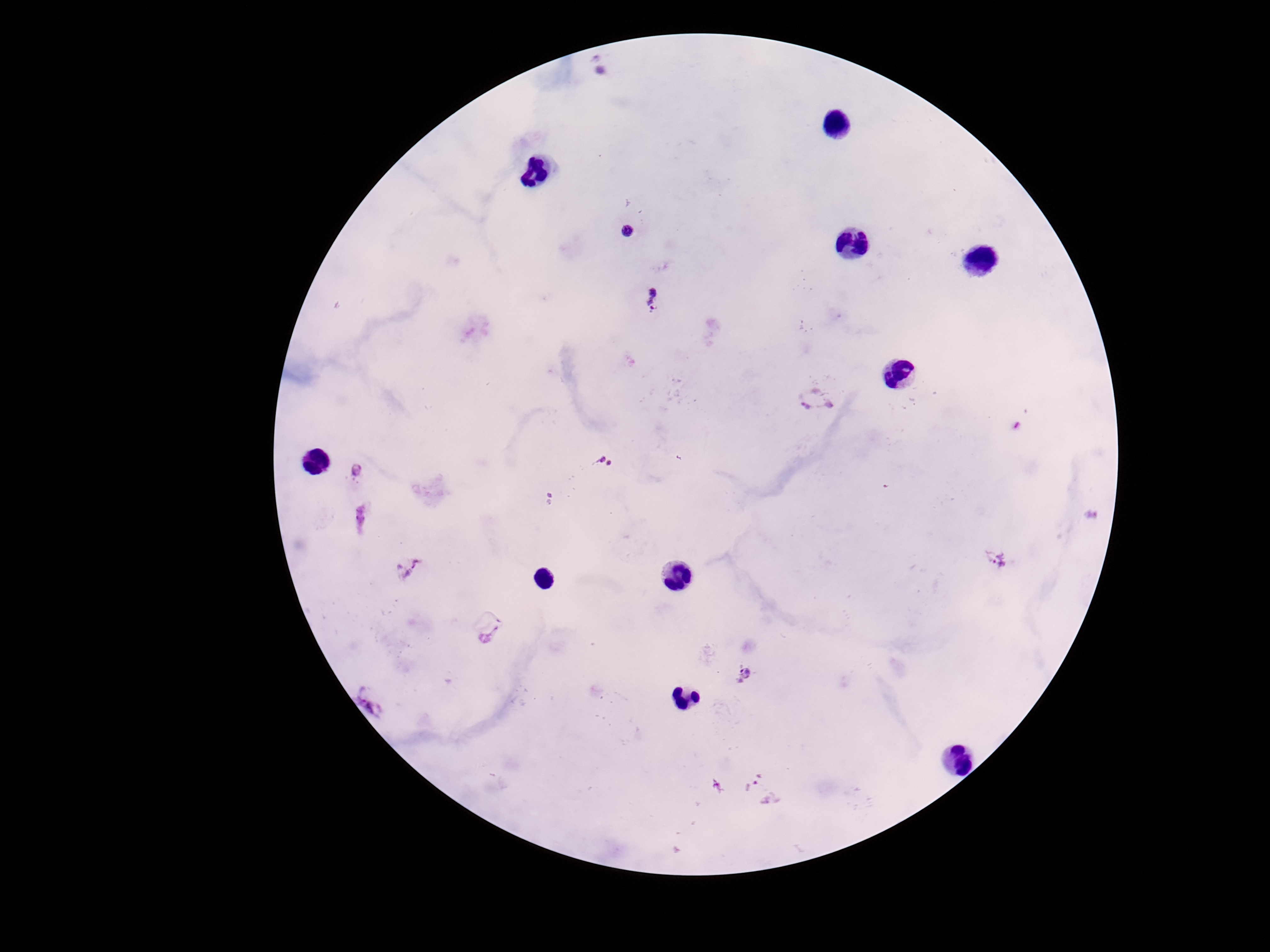
image_size: 1270×952 pixels
patient_malaria_status: infected
preparation: thick blood film
plasmodium_parasite_locations: 'approximate centers as (x, y) in pixels: (599, 65), (626, 230), (653, 299), (814, 397), (602, 464), (357, 468), (550, 498), (998, 562), (406, 568), (491, 638), (746, 673), (372, 698), (763, 790)'
capture: smartphone camera through the microscope eyepiece
stain: Giemsa
field_of_view: single
magnification: 100x